Locate every malaria parasite and every leukocyte.
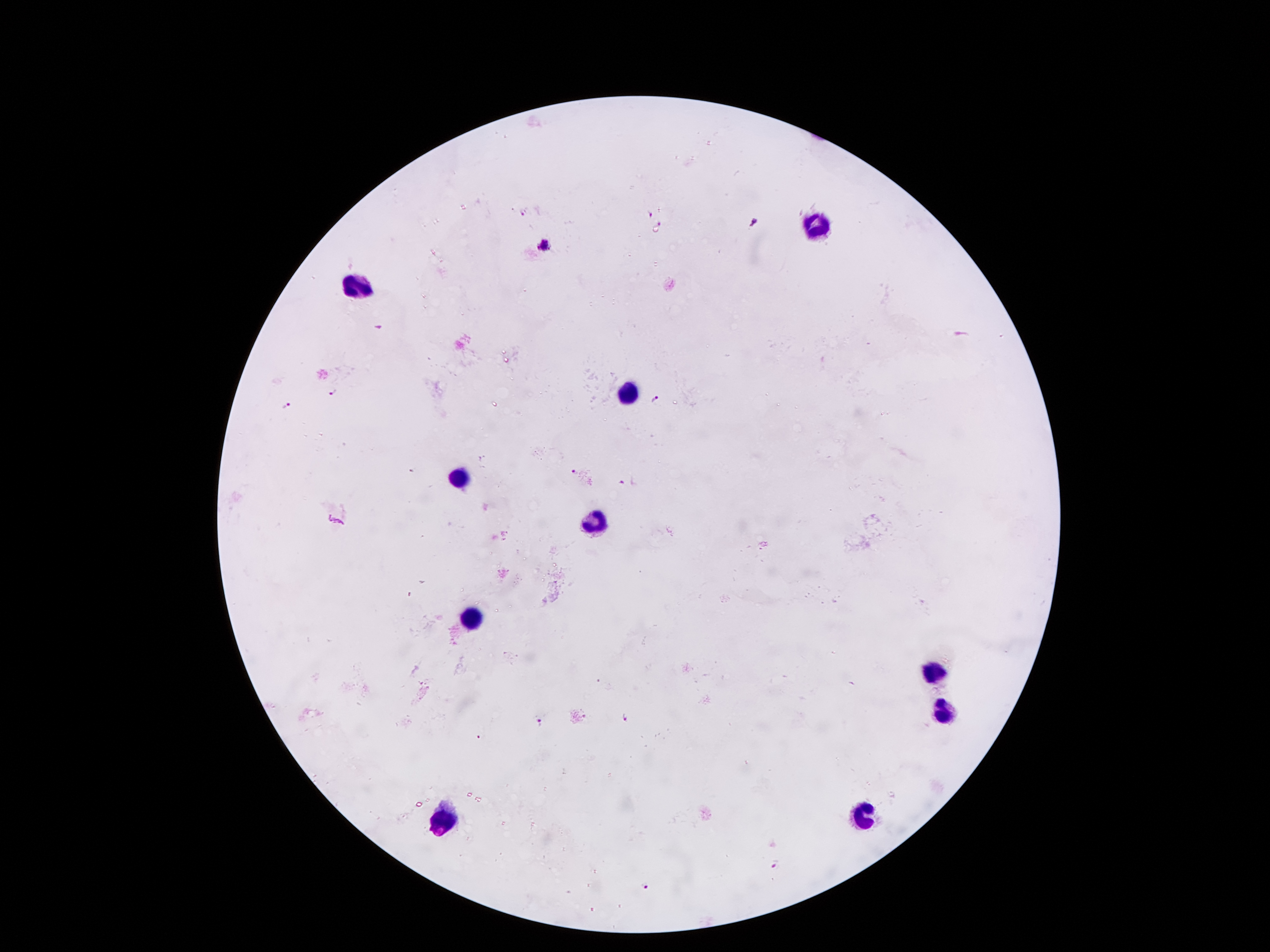

Approximate centers as {x, y} in pixels.
Malaria parasites: {523, 212}, {649, 214}, {755, 220}, {659, 224}, {545, 244}, {332, 390}, {656, 399}, {286, 403}, {575, 471}, {620, 483}, {624, 719}, {540, 720}, {479, 737}, {774, 866}, {644, 886}.
Leukocytes: {819, 227}, {361, 281}, {632, 392}, {452, 476}, {596, 525}, {470, 613}, {930, 672}, {942, 711}, {865, 812}, {445, 817}.

magnification = 100x
stain = Giemsa
field of view = one from this slide
capture = smartphone camera through the microscope eyepiece
image size = 1270×952 pixels
patient malaria status = infected with Plasmodium falciparum
preparation = thick blood film